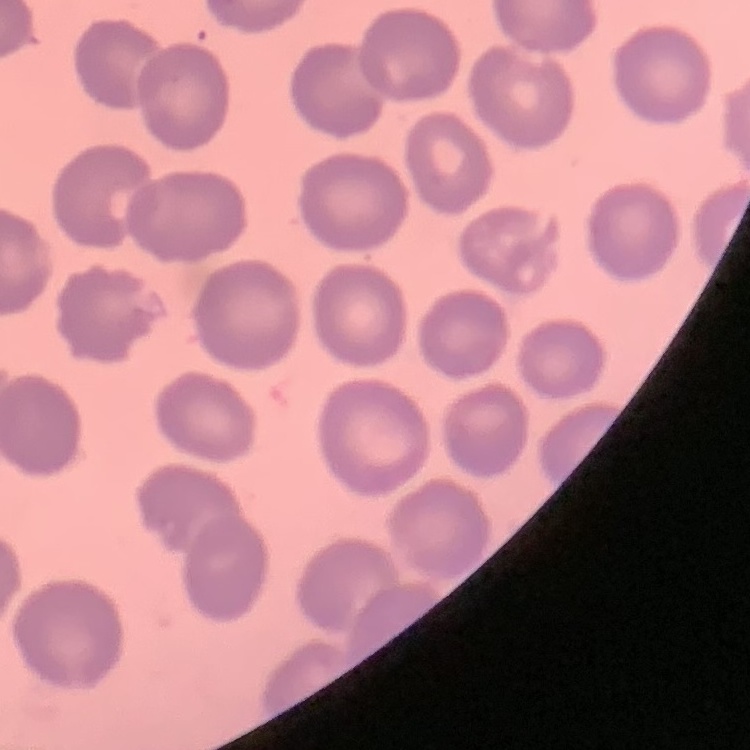
Summary:
  - Erythrocyte morphology: no rouleaux formation
  - Image type: one tile cut from a larger photomicrograph
  - Stain: Field's or Giemsa
  - Preparation: thin blood smear